Assess this cell for malaria.
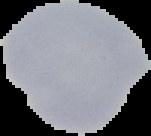

It is uninfected.

{
  "image_size": "151×136 pixels",
  "image_type": "cell region segmented out of the field of view; surrounding area masked to black",
  "preparation": "thin blood smear"
}